Locate every Plasmodium falciparum-infected red blood cell.
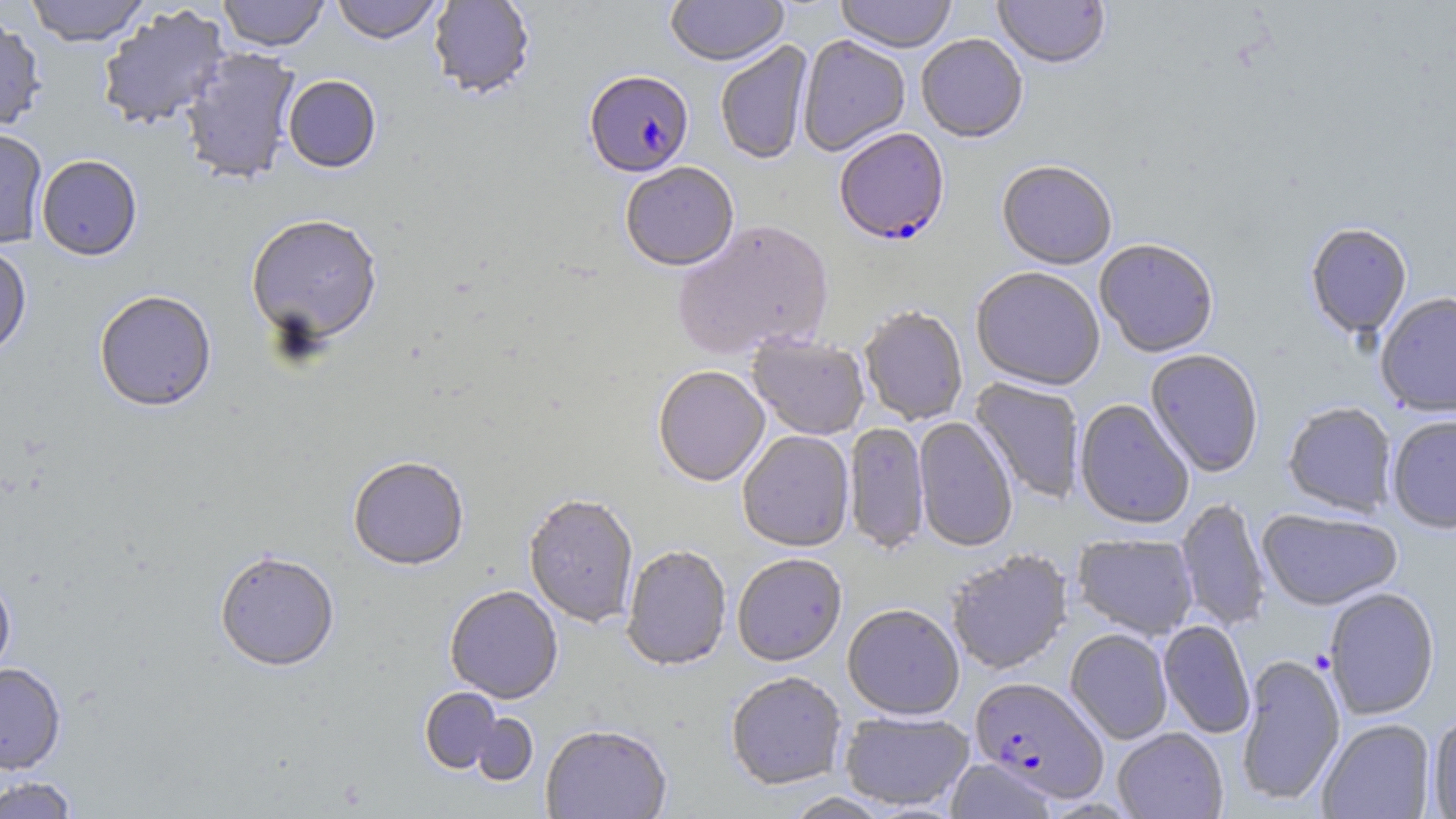
Approximate bounding boxes as [x1, y1, x2, y2] in pixels.
Plasmodium falciparum-infected red blood cells: [584, 72, 694, 180], [834, 130, 950, 248], [970, 678, 1109, 802].

Summary:
  - Uninfected red blood cell locations: [24, 0, 151, 46], [217, 0, 330, 52], [330, 0, 443, 45], [428, 0, 535, 101], [665, 0, 788, 69], [835, 0, 957, 55], [992, 0, 1110, 71], [96, 4, 231, 132], [0, 11, 47, 133], [797, 36, 910, 157], [916, 36, 1028, 145], [715, 41, 814, 166], [179, 47, 301, 186], [282, 75, 381, 174], [0, 126, 48, 249], [36, 155, 143, 261], [997, 163, 1117, 272], [621, 164, 739, 273], [245, 216, 383, 350], [673, 221, 835, 361], [1305, 224, 1412, 341], [1095, 241, 1218, 359], [0, 244, 32, 360], [971, 269, 1104, 392], [94, 291, 217, 413], [1376, 294, 1456, 417], [859, 308, 968, 426], [747, 336, 869, 441], [1145, 350, 1264, 478], [653, 367, 770, 488], [970, 378, 1085, 503], [1074, 400, 1194, 530], [1282, 402, 1397, 517], [1387, 416, 1456, 535], [914, 417, 1018, 553], [844, 423, 929, 556], [738, 431, 855, 553], [348, 458, 469, 573], [523, 496, 638, 629], [1176, 499, 1270, 632], [1257, 509, 1403, 612], [1072, 534, 1198, 640], [621, 546, 732, 672], [946, 551, 1073, 675], [215, 554, 340, 673], [733, 555, 847, 668], [0, 576, 16, 683], [444, 587, 563, 705], [1323, 588, 1440, 720], [842, 606, 964, 722], [1158, 620, 1255, 738], [1065, 629, 1172, 745], [1235, 655, 1346, 807], [0, 663, 66, 775], [726, 673, 847, 791], [420, 688, 501, 773], [840, 711, 975, 811], [469, 713, 537, 787], [1426, 713, 1456, 818], [1317, 719, 1435, 819], [541, 726, 672, 819], [1113, 728, 1228, 819], [945, 759, 1059, 819], [0, 775, 81, 819], [780, 792, 895, 819]
  - Slide-level diagnosis: Plasmodium falciparum
  - Modality: light microscopy
  - Field of view: single
  - Magnification: 1000x
  - Stain: May-Grünwald-Giemsa
  - Preparation: thin blood film
  - Image size: 1456×819 pixels